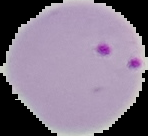
image size = 148×136 pixels
malaria status = parasitized
image type = segmented cell region with the area outside set to black
preparation = thin blood smear